Assess this cell for malaria.
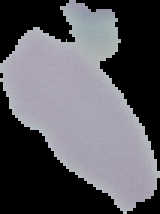
It is uninfected.

Cell region segmented out of the field of view; the surrounding area is masked to black. Image is 160×214 pixels. From a thin blood film.